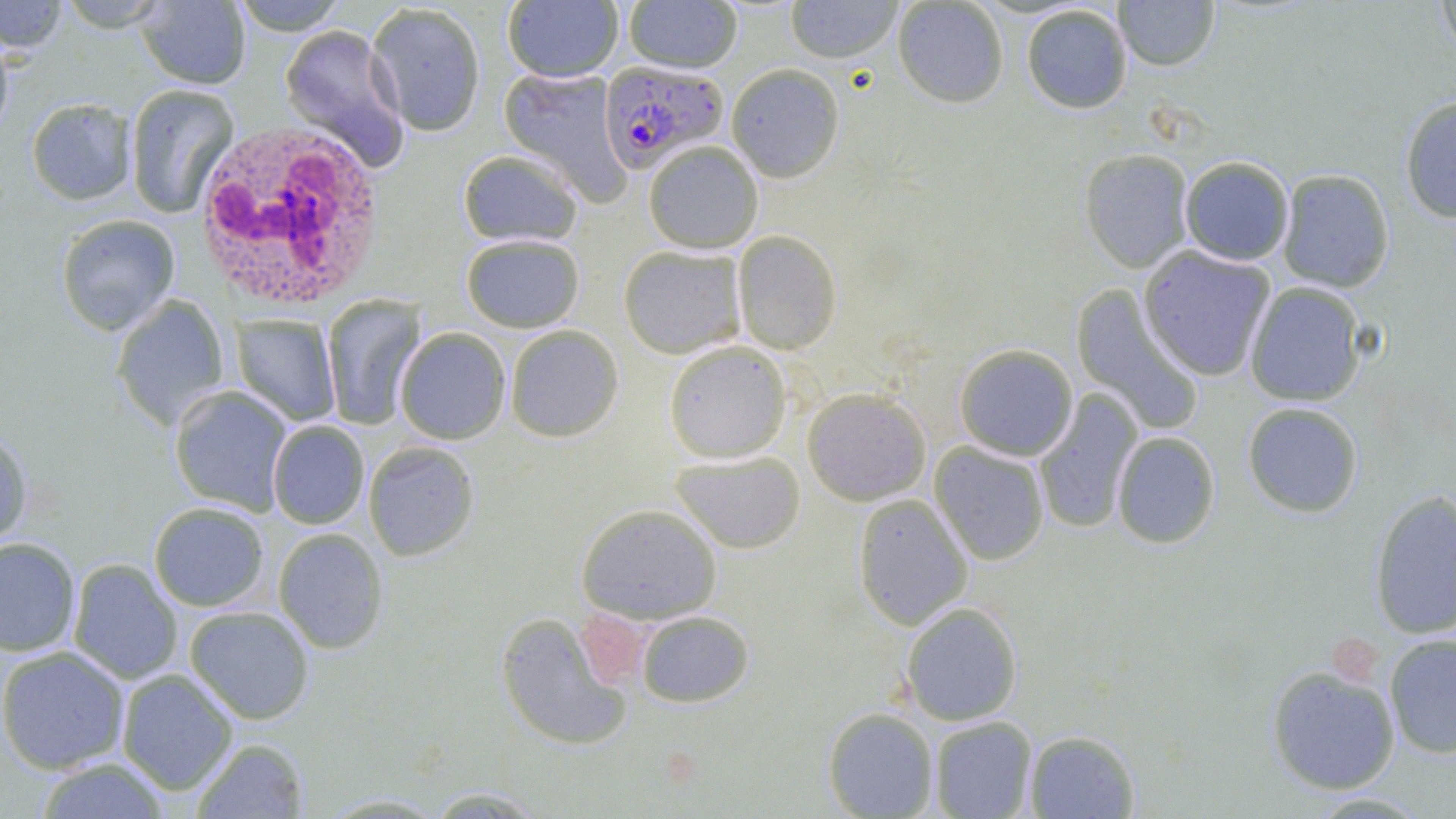
Summary:
  - Coordinate format: approximate bounding boxes as named x1/y1/x2/y2 corners in pixels
  - Uninfected red blood cell locations: (x1=0, y1=0, x2=69, y2=53), (x1=137, y1=0, x2=251, y2=89), (x1=231, y1=0, x2=349, y2=35), (x1=624, y1=0, x2=743, y2=73), (x1=785, y1=0, x2=902, y2=63), (x1=893, y1=0, x2=1009, y2=108), (x1=1113, y1=0, x2=1219, y2=71), (x1=1436, y1=0, x2=1456, y2=60), (x1=53, y1=1, x2=173, y2=32), (x1=502, y1=1, x2=624, y2=83), (x1=366, y1=3, x2=486, y2=136), (x1=1021, y1=4, x2=1133, y2=114), (x1=280, y1=24, x2=409, y2=169), (x1=0, y1=33, x2=15, y2=143), (x1=726, y1=63, x2=845, y2=182), (x1=499, y1=67, x2=631, y2=205), (x1=124, y1=84, x2=239, y2=219), (x1=1400, y1=96, x2=1456, y2=224), (x1=26, y1=98, x2=137, y2=205), (x1=643, y1=140, x2=764, y2=254), (x1=1079, y1=148, x2=1194, y2=273), (x1=457, y1=149, x2=584, y2=248), (x1=1180, y1=156, x2=1294, y2=265), (x1=1277, y1=169, x2=1395, y2=293), (x1=56, y1=214, x2=180, y2=335), (x1=732, y1=230, x2=842, y2=355), (x1=461, y1=234, x2=585, y2=333), (x1=618, y1=245, x2=746, y2=359), (x1=1138, y1=246, x2=1275, y2=381), (x1=1245, y1=282, x2=1366, y2=406), (x1=1071, y1=285, x2=1204, y2=436), (x1=111, y1=295, x2=229, y2=431), (x1=322, y1=295, x2=426, y2=430), (x1=231, y1=314, x2=341, y2=426), (x1=505, y1=325, x2=624, y2=442), (x1=395, y1=327, x2=511, y2=444), (x1=664, y1=341, x2=792, y2=463), (x1=954, y1=343, x2=1078, y2=461), (x1=169, y1=385, x2=292, y2=515), (x1=803, y1=388, x2=931, y2=505), (x1=1034, y1=390, x2=1143, y2=534), (x1=1242, y1=402, x2=1363, y2=517), (x1=267, y1=421, x2=369, y2=529), (x1=0, y1=427, x2=33, y2=550), (x1=1112, y1=431, x2=1220, y2=549), (x1=364, y1=441, x2=480, y2=561), (x1=930, y1=442, x2=1050, y2=566), (x1=670, y1=451, x2=805, y2=553), (x1=1369, y1=488, x2=1456, y2=639), (x1=853, y1=494, x2=973, y2=630), (x1=149, y1=502, x2=269, y2=611), (x1=576, y1=503, x2=722, y2=624), (x1=273, y1=528, x2=389, y2=653), (x1=0, y1=537, x2=81, y2=657), (x1=68, y1=559, x2=183, y2=684), (x1=901, y1=602, x2=1022, y2=726), (x1=184, y1=606, x2=315, y2=724), (x1=636, y1=610, x2=754, y2=708), (x1=495, y1=612, x2=635, y2=751), (x1=1385, y1=633, x2=1456, y2=758), (x1=0, y1=646, x2=130, y2=774), (x1=1266, y1=665, x2=1401, y2=795), (x1=116, y1=669, x2=238, y2=795), (x1=823, y1=707, x2=939, y2=818), (x1=929, y1=716, x2=1037, y2=819), (x1=1024, y1=730, x2=1140, y2=818), (x1=191, y1=738, x2=309, y2=818), (x1=35, y1=757, x2=172, y2=818), (x1=421, y1=787, x2=550, y2=817)
  - White blood cell locations: (x1=192, y1=120, x2=387, y2=312)
  - Plasmodium falciparum-infected red blood cell locations: (x1=597, y1=60, x2=728, y2=173)
  - Platelet locations: (x1=575, y1=612, x2=653, y2=682), (x1=1334, y1=639, x2=1382, y2=686)
  - Slide-level diagnosis: Plasmodium falciparum
  - Preparation: thin blood smear
  - Magnification: 1000x
  - Image size: 1456×819 pixels
  - Field of view: one of a larger specimen
  - Modality: optical microscopy
  - Stain: May-Grünwald-Giemsa